State which cell type is depicted.
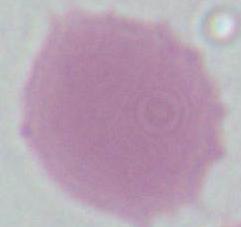
This is an erythrocyte.

Summary:
  - Magnification: 1000x
  - Modality: micrograph